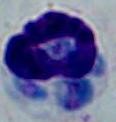
identification = white blood cell
magnification = 1000x
modality = micrograph